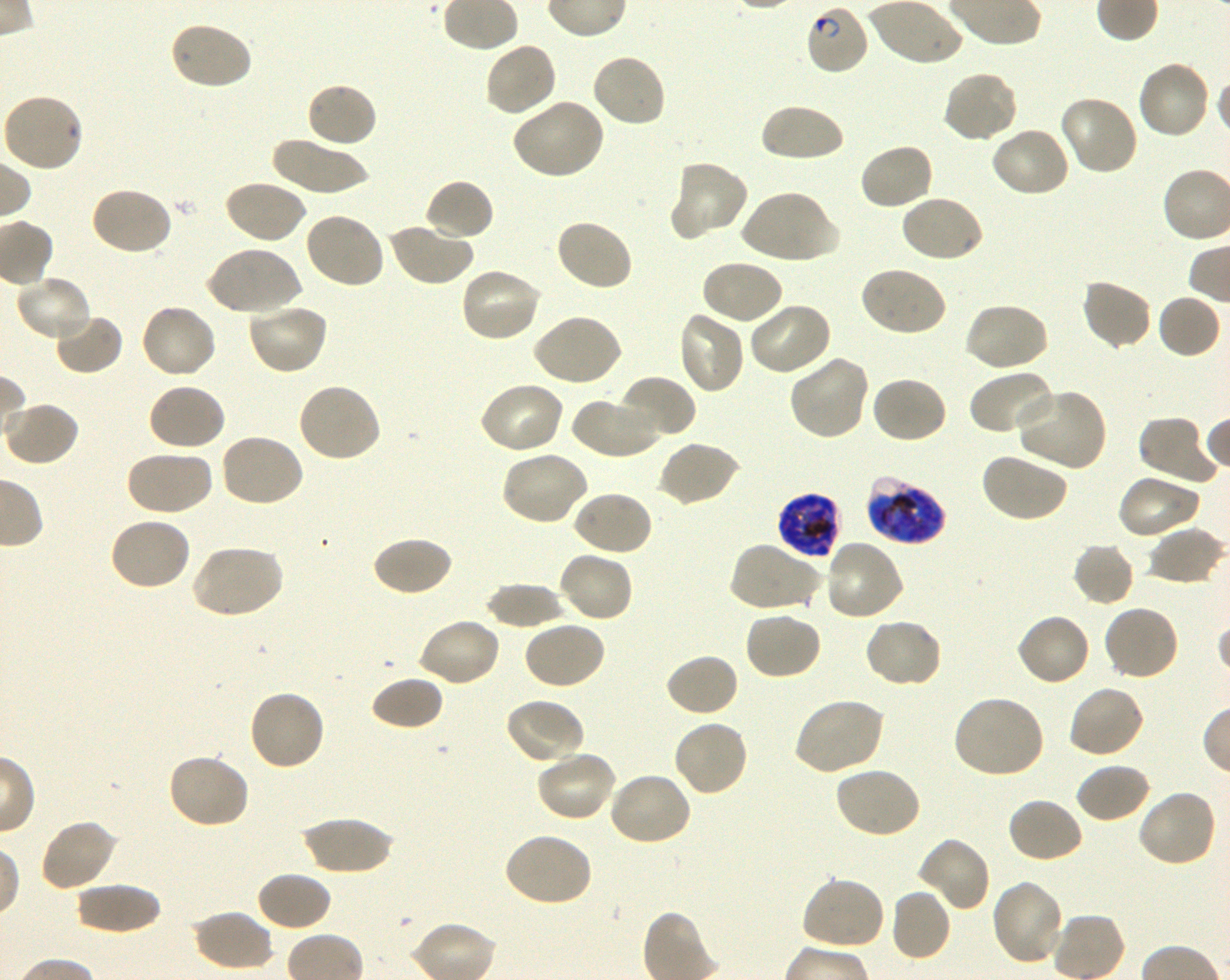

Approximate bounding boxes as {x1, y1, x2, y2} in pixels. Not every red blood cell is marked. A life-cycle stage — or a range of stages, where the recorded stages span more than one — follows each staged infected red blood cell.
Summary:
  - Locations of infected red blood cells: {805, 4, 871, 77} ring; {867, 476, 947, 545} late trophozoite to late schizont; {776, 491, 842, 559} late trophozoite to late schizont
  - Locations of uninfected red blood cells: {168, 20, 253, 92}, {483, 42, 558, 118}, {590, 52, 667, 128}, {1135, 59, 1211, 141}, {942, 69, 1019, 143}, {305, 81, 378, 150}, {3, 93, 85, 173}, {1058, 95, 1140, 177}, {510, 98, 606, 180}, {758, 102, 846, 164}, {990, 125, 1071, 199}, {270, 137, 370, 194}, {858, 142, 936, 211}, {670, 160, 750, 239}, {423, 177, 495, 242}, {223, 179, 307, 245}, {88, 186, 173, 257}, {738, 189, 836, 266}, {899, 193, 985, 264}, {304, 211, 387, 290}, {553, 218, 634, 293}, {386, 222, 474, 287}, {206, 245, 302, 316}, {699, 259, 785, 326}, {459, 266, 544, 343}, {858, 266, 948, 338}, {14, 277, 93, 344}, {1079, 279, 1153, 351}, {1156, 293, 1222, 359}, {746, 300, 833, 376}, {245, 301, 330, 376}, {963, 301, 1049, 373}, {139, 303, 218, 380}, {676, 310, 746, 395}, {51, 312, 124, 376}, {531, 313, 623, 387}, {788, 354, 870, 440}, {968, 368, 1057, 437}, {619, 374, 696, 441}, {870, 376, 948, 444}, {478, 380, 566, 455}, {147, 382, 227, 452}, {295, 382, 381, 464}, {1015, 387, 1106, 472}, {569, 394, 661, 459}, {3, 401, 80, 467}, {1137, 414, 1219, 488}, {218, 433, 306, 509}, {657, 440, 741, 508}, {125, 449, 213, 517}, {499, 450, 590, 527}, {980, 451, 1069, 523}, {1116, 472, 1202, 540}, {570, 490, 653, 557}, {109, 515, 192, 591}, {1147, 527, 1226, 586}, {371, 535, 453, 598}, {823, 540, 905, 623}, {728, 541, 822, 613}, {1073, 542, 1136, 607}, {189, 544, 284, 619}, {557, 550, 635, 624}, {484, 583, 569, 630}, {1102, 603, 1181, 681}, {744, 608, 823, 681}, {1015, 612, 1093, 688}, {417, 617, 502, 688}, {863, 617, 944, 688}, {521, 620, 607, 691}, {664, 653, 740, 718}, {369, 675, 444, 731}, {1066, 683, 1146, 759}, {247, 688, 327, 771}, {951, 694, 1046, 780}, {504, 697, 586, 766}, {792, 697, 885, 776}, {672, 719, 750, 798}, {535, 749, 618, 823}, {167, 752, 251, 830}, {1074, 762, 1151, 824}, {833, 766, 922, 840}, {607, 770, 693, 846}, {1137, 788, 1218, 867}, {1006, 797, 1083, 864}, {300, 816, 397, 874}, {37, 819, 118, 892}, {501, 832, 594, 908}, {916, 836, 991, 913}, {255, 870, 333, 932}, {800, 875, 887, 951}, {990, 879, 1066, 967}, {74, 883, 164, 935}, {889, 887, 952, 963}, {192, 909, 274, 972}
  - Stain: Giemsa
  - Objective: 100x, oil immersion, numerical aperture 1.30
  - Field of view: one from this slide
  - Culture: Plasmodium falciparum strain 3D7, shaking, in vitro
  - Donor blood group: O+
  - Image size: 1230×980 pixels
  - Preparation: thin blood film